Identify the parasite.
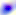

This is Toxoplasma gondii.

Summary:
  - Magnification: 400x
  - Modality: micrograph